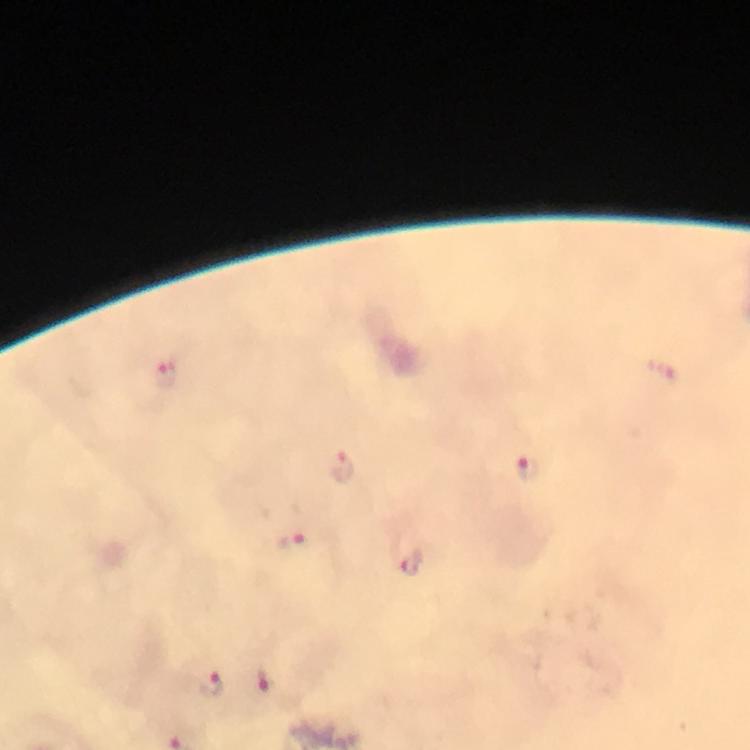
Approximate centers as (x, y) in pixels.
Summary:
  - Plasmodium parasite locations: (165, 371), (342, 465), (528, 467), (293, 540), (411, 562), (265, 679), (210, 683)
  - Preparation: thick smear
  - Immersion oil: used
  - Capture: smartphone mounted on the microscope
  - Stain: Giemsa
  - Magnification: 100x
  - Context: from a diagnostic examination for malaria
  - Image size: 750×750 pixels
  - Cropped from: one field of view